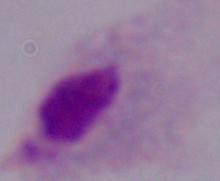
A trichomonad is shown. Photomicrograph. 1000x magnification.